Describe the morphology of the red blood cells.
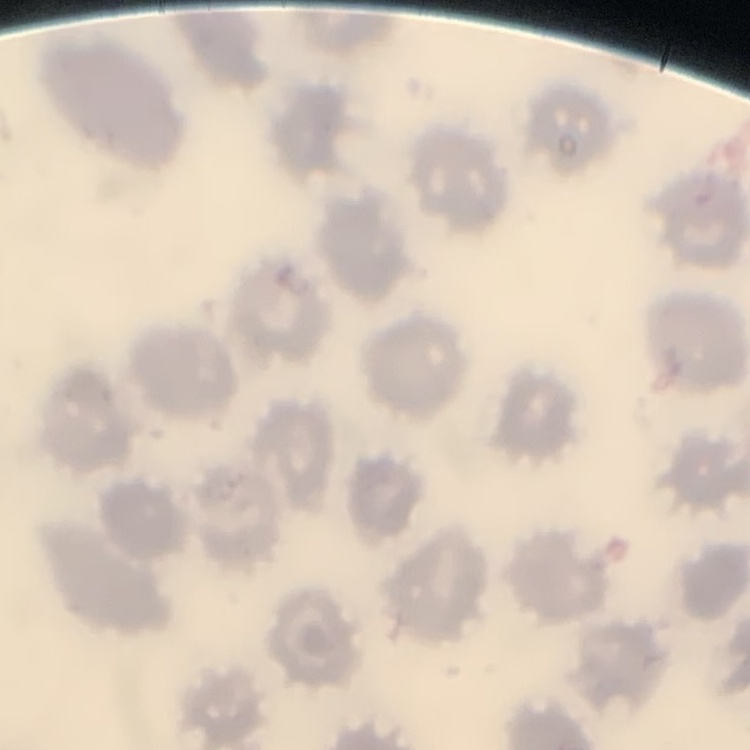
They show no rouleaux formation.

Stained with either Field's or Giemsa. Thin blood smear. Square crop of a larger photomicrograph.